Report the malaria status of this cell.
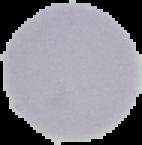

Uninfected.

Image is 142×145 pixels. From a thin blood film. Cell region segmented out of the field of view; the surrounding area is masked to black.